Report the malaria status of this cell.
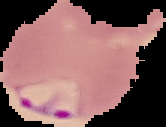

It is parasitized.

Summary:
  - Image size: 166×127 pixels
  - Preparation: thin blood smear
  - Image type: segmented cell region on a black background